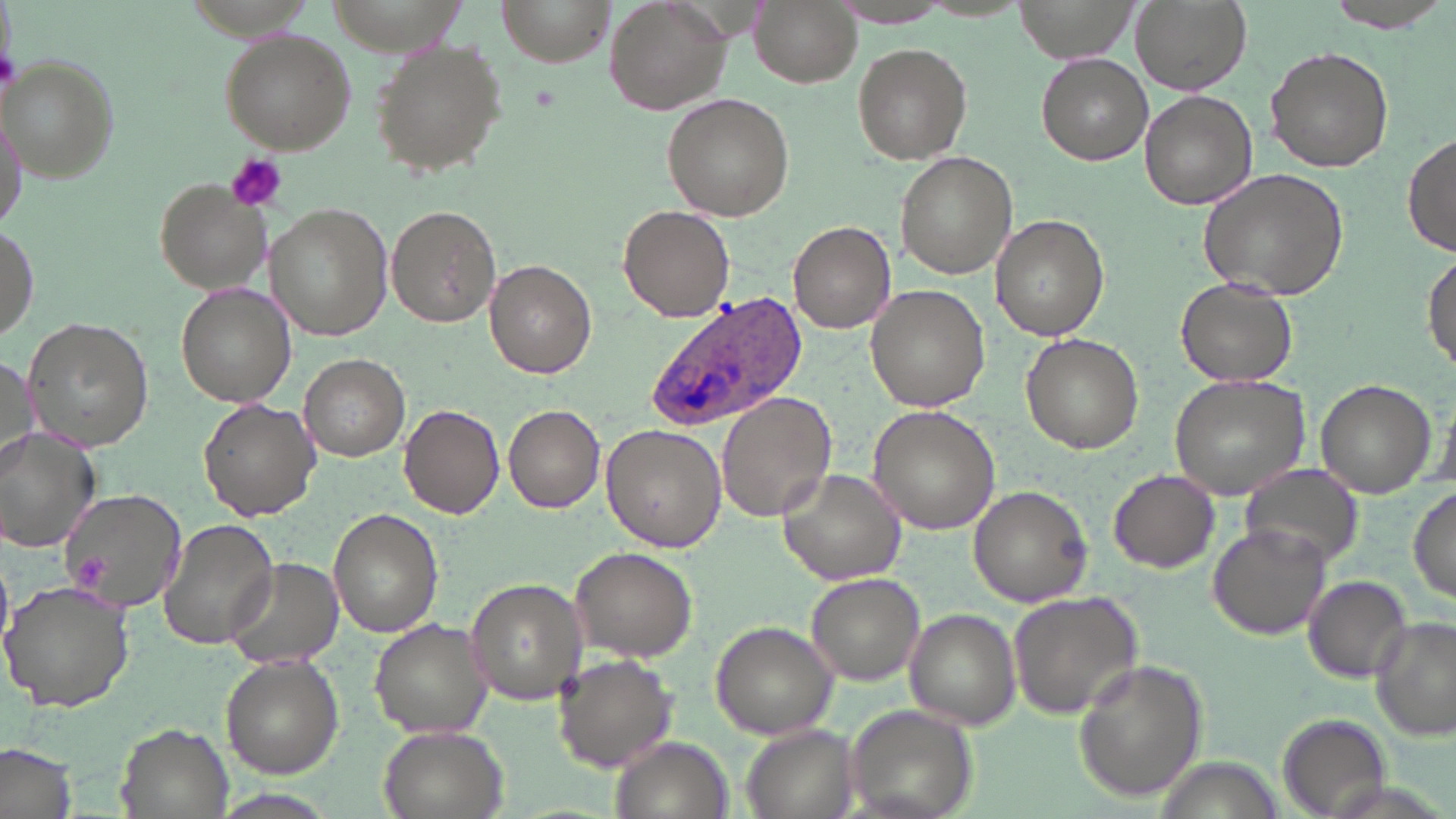
Summary:
  - Coordinate format: approximate bounding boxes as [x1, y1, x2, y2] in pixels
  - Plasmodium ovale-infected red blood cell locations: [646, 288, 808, 432]
  - Uninfected red blood cell locations: [497, 0, 614, 68], [600, 0, 734, 116], [752, 0, 861, 87], [1015, 0, 1135, 62], [1130, 0, 1253, 98], [1324, 0, 1450, 28], [826, 2, 954, 29], [219, 29, 356, 154], [371, 38, 507, 177], [852, 41, 972, 164], [1264, 46, 1394, 173], [1036, 54, 1154, 166], [4, 60, 118, 182], [1138, 90, 1257, 210], [662, 94, 794, 220], [0, 100, 27, 234], [1402, 133, 1456, 257], [894, 151, 1017, 280], [1196, 168, 1351, 301], [155, 180, 268, 294], [266, 203, 392, 340], [387, 204, 503, 329], [618, 204, 735, 321], [992, 215, 1109, 340], [1, 219, 38, 347], [788, 219, 896, 332], [1424, 248, 1456, 373], [484, 260, 595, 379], [1175, 278, 1298, 387], [174, 283, 296, 407], [865, 283, 989, 410], [23, 318, 153, 451], [1021, 334, 1146, 455], [0, 352, 34, 479], [299, 354, 409, 461], [1169, 371, 1314, 500], [1316, 380, 1436, 497], [716, 393, 837, 520], [199, 399, 320, 519], [399, 404, 504, 518], [503, 404, 604, 511], [869, 406, 998, 535], [601, 426, 726, 552], [1, 429, 100, 552], [1242, 466, 1362, 568], [777, 467, 909, 584], [1108, 468, 1220, 572], [968, 484, 1093, 607], [1410, 485, 1455, 606], [57, 487, 185, 615], [330, 509, 444, 637], [156, 519, 280, 649], [1208, 524, 1329, 640], [572, 547, 694, 660], [223, 557, 342, 671], [805, 571, 927, 685], [1304, 575, 1412, 682], [465, 577, 588, 707], [2, 578, 134, 713], [1007, 591, 1143, 721], [905, 609, 1021, 730], [1371, 616, 1455, 741], [369, 618, 493, 737], [711, 621, 839, 739], [553, 653, 677, 771], [219, 655, 342, 778], [1072, 659, 1209, 803], [845, 706, 979, 819], [1275, 712, 1393, 817], [116, 722, 235, 819], [375, 723, 510, 819], [741, 726, 858, 819], [610, 735, 735, 819], [0, 742, 78, 819]
  - Platelet locations: [0, 44, 20, 93], [226, 153, 288, 213]
  - Slide-level diagnosis: Plasmodium ovale
  - Modality: optical microscopy
  - Field of view: single
  - Preparation: thin blood film
  - Image size: 1456×819 pixels
  - Magnification: 1000x
  - Stain: May-Grünwald-Giemsa